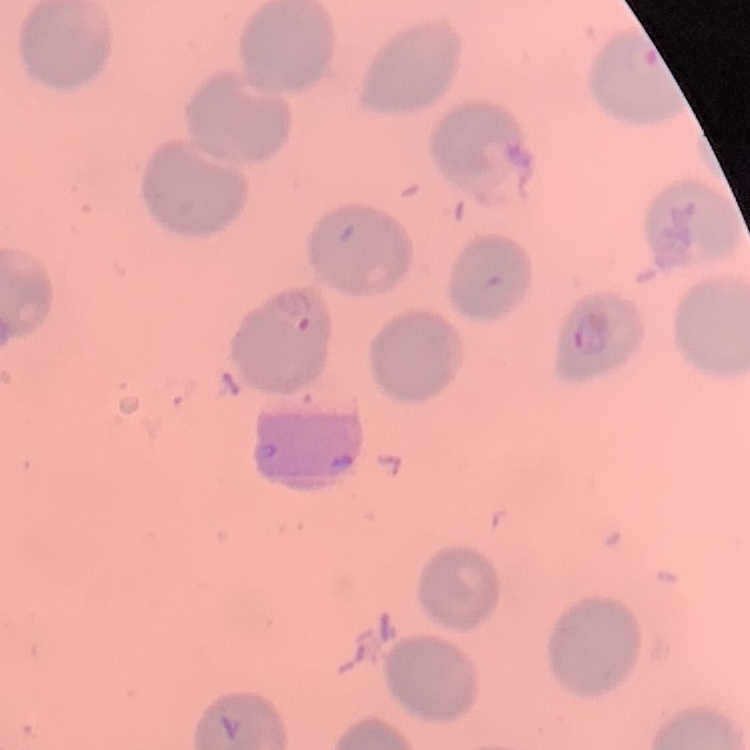

erythrocyte_morphology: no rouleaux formation
preparation: thin peripheral smear
image_type: one tile cut from a larger photomicrograph
stain: Field's or Giemsa